Outline each blood parasite and name the species.
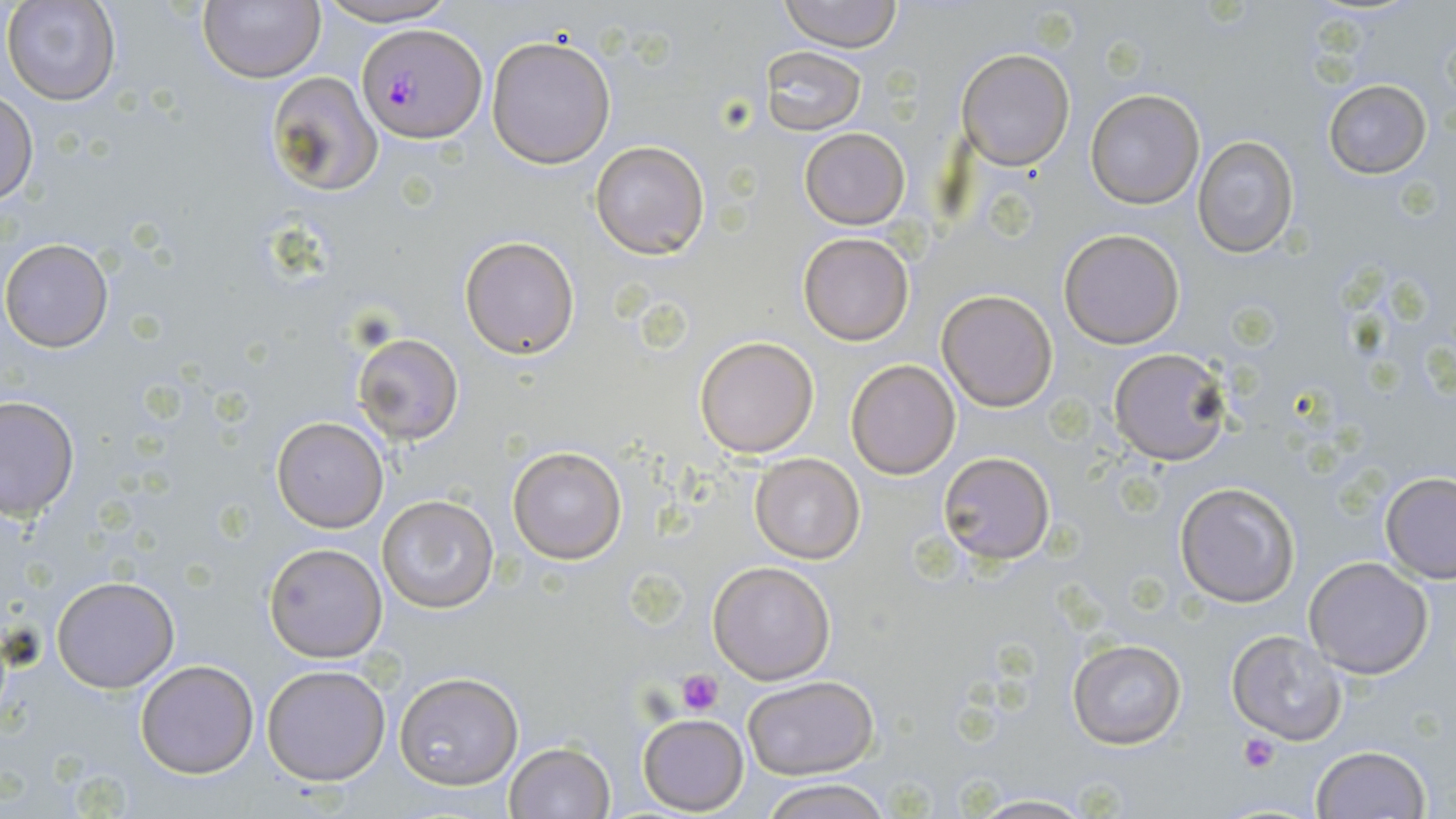

Approximate bounding boxes as (x1,y1)-(x2,y2) corner pairs in pixels.
Plasmodium falciparum-infected red blood cells: (357,22)-(488,143).
No Plasmodium ovale, Plasmodium malariae, Plasmodium vivax, Babesia divergens, or Trypanosoma brucei observed.

Platelet locations: (675,668)-(724,717), (1239,733)-(1279,772). Uninfected red blood cell locations: (2,0)-(123,107), (313,0)-(464,27), (777,0)-(903,51), (198,1)-(324,83), (485,35)-(617,169), (762,45)-(868,135), (956,47)-(1074,170), (263,72)-(382,196), (1323,79)-(1432,178), (0,89)-(37,204), (1084,90)-(1205,209), (799,127)-(911,229), (1192,136)-(1298,257), (590,139)-(710,260), (1058,228)-(1184,349), (798,233)-(915,346), (459,235)-(581,358), (1,239)-(114,353), (935,288)-(1058,411), (350,331)-(466,444), (695,336)-(819,456), (1106,347)-(1235,465), (846,359)-(961,479), (1,395)-(78,520), (273,418)-(388,532), (507,445)-(627,564), (938,452)-(1053,565), (749,453)-(865,564), (1379,472)-(1456,581), (1174,480)-(1300,607), (377,494)-(498,613), (262,541)-(388,662), (1303,556)-(1435,678), (707,560)-(836,683), (51,573)-(181,693), (1227,630)-(1349,746), (1067,639)-(1186,750), (136,659)-(259,779), (262,663)-(392,786), (393,673)-(524,790), (740,675)-(879,779), (637,713)-(748,815), (504,740)-(614,818), (1311,744)-(1431,819), (760,779)-(889,819), (958,793)-(1100,818). Slide-level diagnosis: Plasmodium falciparum. Light microscopy. Single field of view. May-Grünwald-Giemsa-stained preparation. 1000x magnification. Image is 1456×819 pixels. Thin blood smear.